Report the malaria status of this cell.
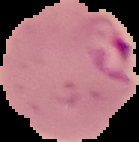

Parasitized.

{
  "image_size": "139×142 pixels",
  "image_type": "segmented cell region with the area outside set to black",
  "preparation": "thin blood smear"
}